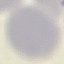
Malaria status: uninfected. Thin blood film. Automatically extracted cell patch, resized to 64 × 64 pixels. Giemsa-stained preparation. Acquired by smartphone through the microscope eyepiece.